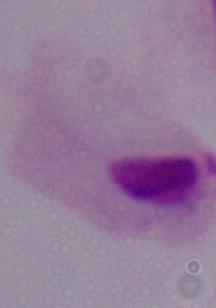

magnification = 1000x
modality = micrograph
identification = trichomonad